Classify this cell by malaria status.
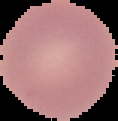
Uninfected.

From a thin blood smear. Image is 118×121 pixels. The area outside the segmented cell region is set to black.